Outline each blood parasite and name the species.
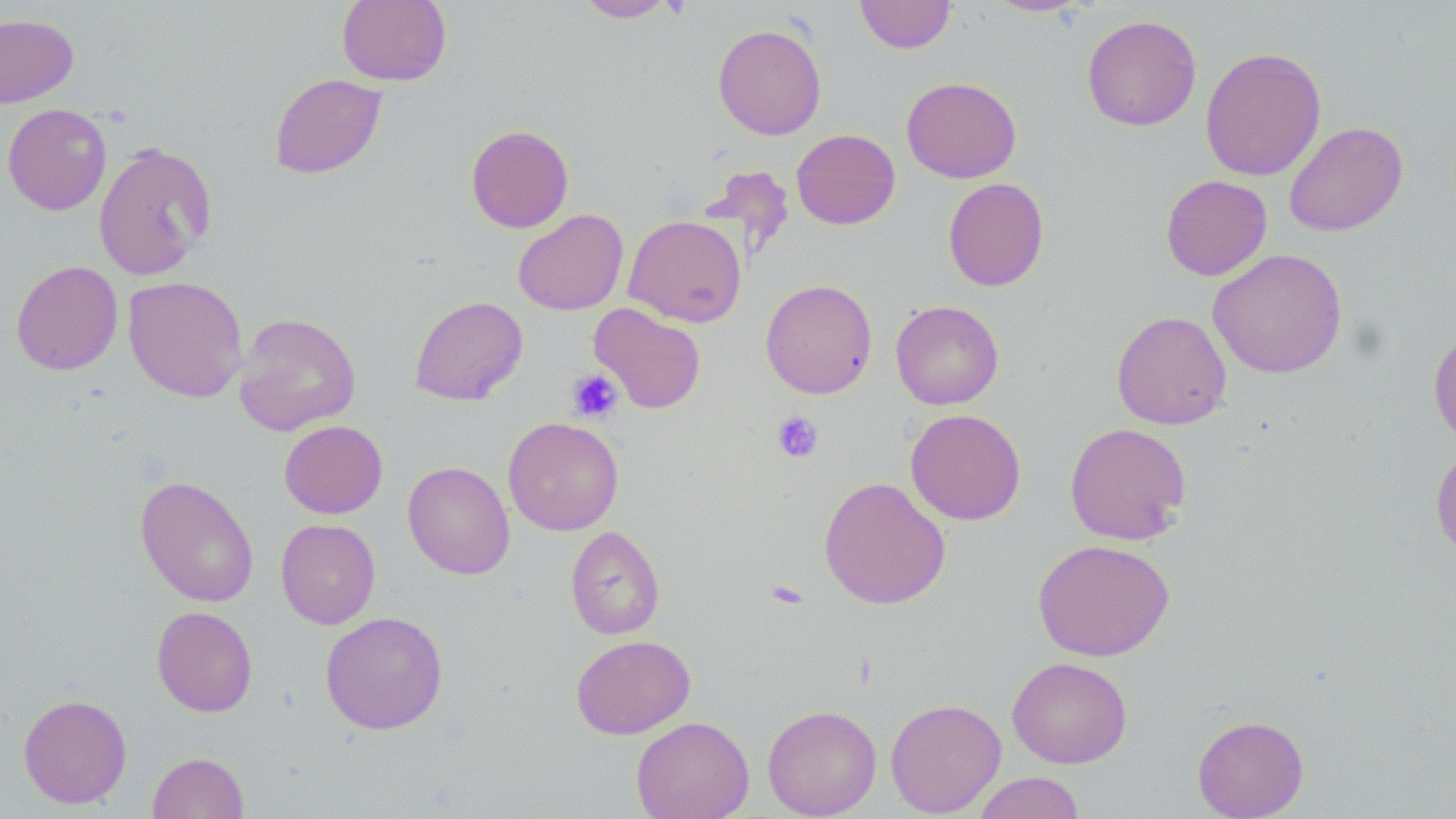
No blood parasites observed.

Approximate bounding boxes as (x1, y1, x2, y2) in pixels. Platelet locations: (567, 369, 623, 423), (772, 411, 823, 463), (764, 577, 810, 611). Uninfected red blood cell locations: (337, 0, 451, 86), (575, 0, 676, 22), (854, 0, 955, 54), (986, 0, 1088, 17), (0, 12, 79, 107), (1082, 14, 1202, 132), (713, 23, 827, 140), (1200, 47, 1326, 181), (269, 73, 386, 179), (901, 77, 1021, 183), (2, 103, 112, 215), (1284, 121, 1408, 237), (466, 124, 574, 233), (791, 128, 901, 230), (93, 141, 217, 280), (1161, 175, 1272, 281), (943, 177, 1049, 291), (513, 209, 628, 315), (623, 214, 747, 327), (1208, 248, 1348, 378), (11, 260, 123, 375), (123, 276, 248, 402), (760, 279, 877, 398), (409, 295, 528, 406), (890, 300, 1004, 409), (589, 303, 706, 414), (1112, 310, 1232, 430), (234, 312, 362, 436), (1428, 324, 1456, 449), (905, 409, 1026, 525), (503, 416, 624, 535), (279, 420, 388, 519), (1065, 422, 1192, 545), (1430, 444, 1456, 564), (402, 461, 515, 579), (135, 475, 259, 607), (818, 476, 951, 609), (276, 518, 380, 628), (565, 525, 665, 640), (1032, 539, 1176, 662), (152, 606, 258, 717), (320, 611, 448, 735), (570, 634, 695, 739), (1007, 656, 1132, 768), (18, 693, 132, 809), (885, 698, 1006, 817), (762, 704, 882, 818), (1192, 714, 1309, 818), (631, 716, 755, 819), (147, 752, 249, 818), (972, 771, 1086, 819). Slide-level diagnosis: negative for blood parasites. Thin blood film. Captured at 1000x magnification. Image is 1456×819 pixels. Optical microscopy. May-Grünwald-Giemsa-stained preparation. One field of a larger specimen.